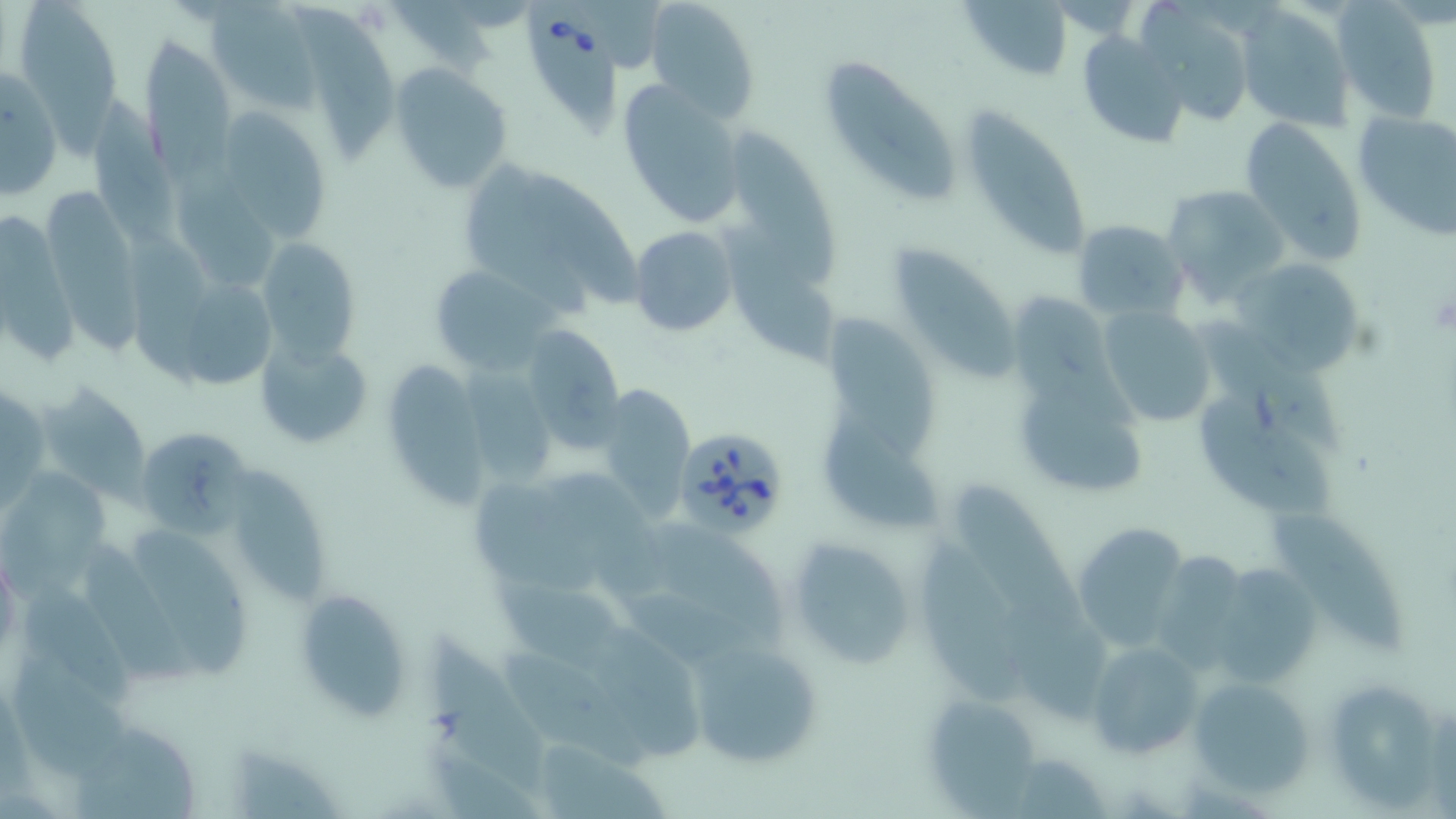
slide-level diagnosis = Babesia divergens
stain = May-Grünwald-Giemsa
Babesia divergens-infected red blood cell locations = approximate bounding boxes as (x1,y1)-(x2,y2) corner pairs in pixels: (524,17)-(627,138), (673,426)-(791,539)
preparation = thin blood film
modality = optical microscopy
uninfected red blood cell locations = approximate bounding boxes as (x1,y1)-(x2,y2) corner pairs in pixels: (585,0)-(663,72), (646,0)-(761,122), (17,2)-(122,158), (961,2)-(1077,81), (1235,3)-(1355,131), (1335,3)-(1444,125), (208,4)-(322,109), (297,5)-(400,172), (1143,9)-(1255,127), (1076,32)-(1193,150), (142,33)-(237,174), (819,55)-(961,204), (389,61)-(515,194), (1,67)-(61,201), (617,78)-(748,230), (89,84)-(180,244), (225,107)-(329,246), (959,108)-(1092,265), (1351,108)-(1456,239), (1238,117)-(1368,267), (728,120)-(835,285), (454,157)-(633,311), (170,169)-(281,287), (1160,183)-(1288,300), (45,184)-(150,361), (2,210)-(85,372), (1072,218)-(1187,320), (723,225)-(841,373), (630,226)-(739,336), (125,228)-(214,395), (259,233)-(357,379), (896,237)-(1018,380), (1237,259)-(1361,377), (427,262)-(553,373), (185,280)-(274,389), (1097,306)-(1214,429), (822,310)-(945,462), (1195,312)-(1353,461), (518,327)-(623,449), (257,337)-(371,446), (392,354)-(493,517), (466,360)-(559,483), (1012,363)-(1147,502), (39,384)-(153,500), (597,385)-(698,522), (0,386)-(48,514), (1195,392)-(1337,520), (822,397)-(943,533), (138,428)-(253,534), (230,460)-(334,607), (550,468)-(670,603), (0,471)-(119,614), (473,476)-(601,591), (955,476)-(1080,624), (1267,511)-(1414,661), (654,521)-(788,646), (1070,522)-(1192,653), (129,524)-(256,686), (919,534)-(1023,712), (786,536)-(918,670), (78,540)-(197,688), (1148,546)-(1241,668), (1219,555)-(1311,682), (489,561)-(625,671), (21,576)-(146,715), (626,585)-(752,672), (293,590)-(411,721), (1006,594)-(1108,718), (427,625)-(546,791), (599,628)-(701,761), (686,635)-(823,770), (502,637)-(651,768), (1084,639)-(1207,761), (9,652)-(132,782), (1187,673)-(1317,797), (1319,675)-(1450,809), (918,691)-(1047,812), (64,730)-(194,819), (540,743)-(673,819), (216,744)-(344,819)
field of view = one of a larger specimen
magnification = 1000x
image size = 1456×819 pixels